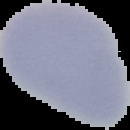 Malaria status: uninfected. From a thin blood smear. Segmented cell region on a black background. Image is 130×130 pixels.